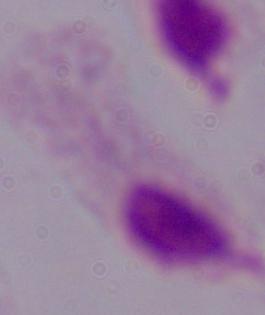

magnification = 1000x
identification = trichomonad
modality = photomicrograph